Point out each leukocyte.
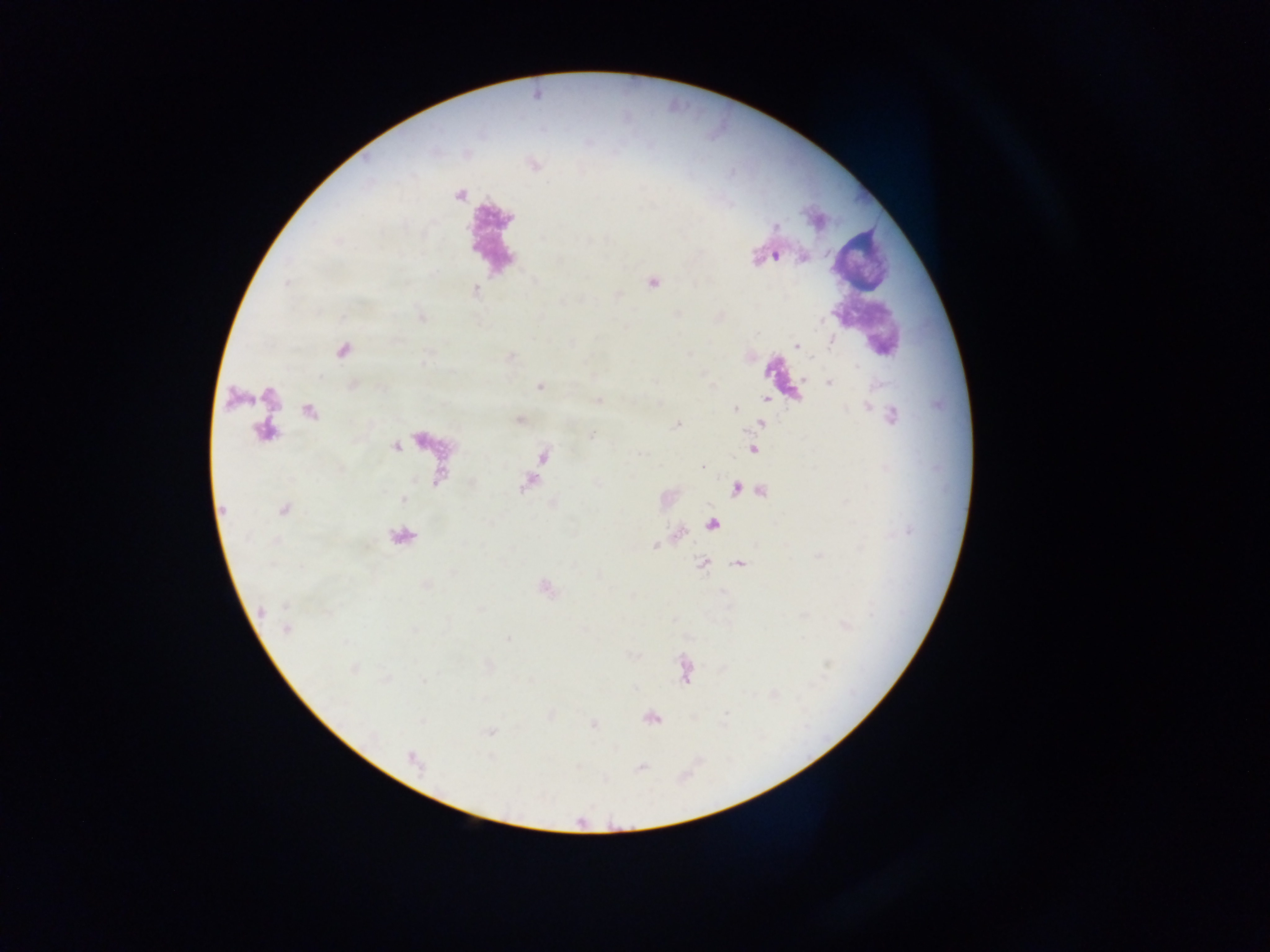
No leukocytes observed.

Approximate centers as (x, y) in pixels. Malaria parasite locations: (778, 227), (756, 256), (776, 257), (654, 281), (476, 290), (618, 296), (822, 319), (832, 343), (796, 344), (803, 379), (655, 382), (830, 382), (538, 386), (598, 399), (867, 407), (734, 408), (893, 418), (676, 424), (591, 434), (702, 466), (534, 479), (761, 491), (655, 545), (425, 586), (260, 611), (287, 629), (413, 631), (726, 712). One field of view. Sample from Ghana. Thick blood smear. Image is 1270×952 pixels. Mobile-phone photograph taken through the microscope.